Locate every leukocyte (white blood cell).
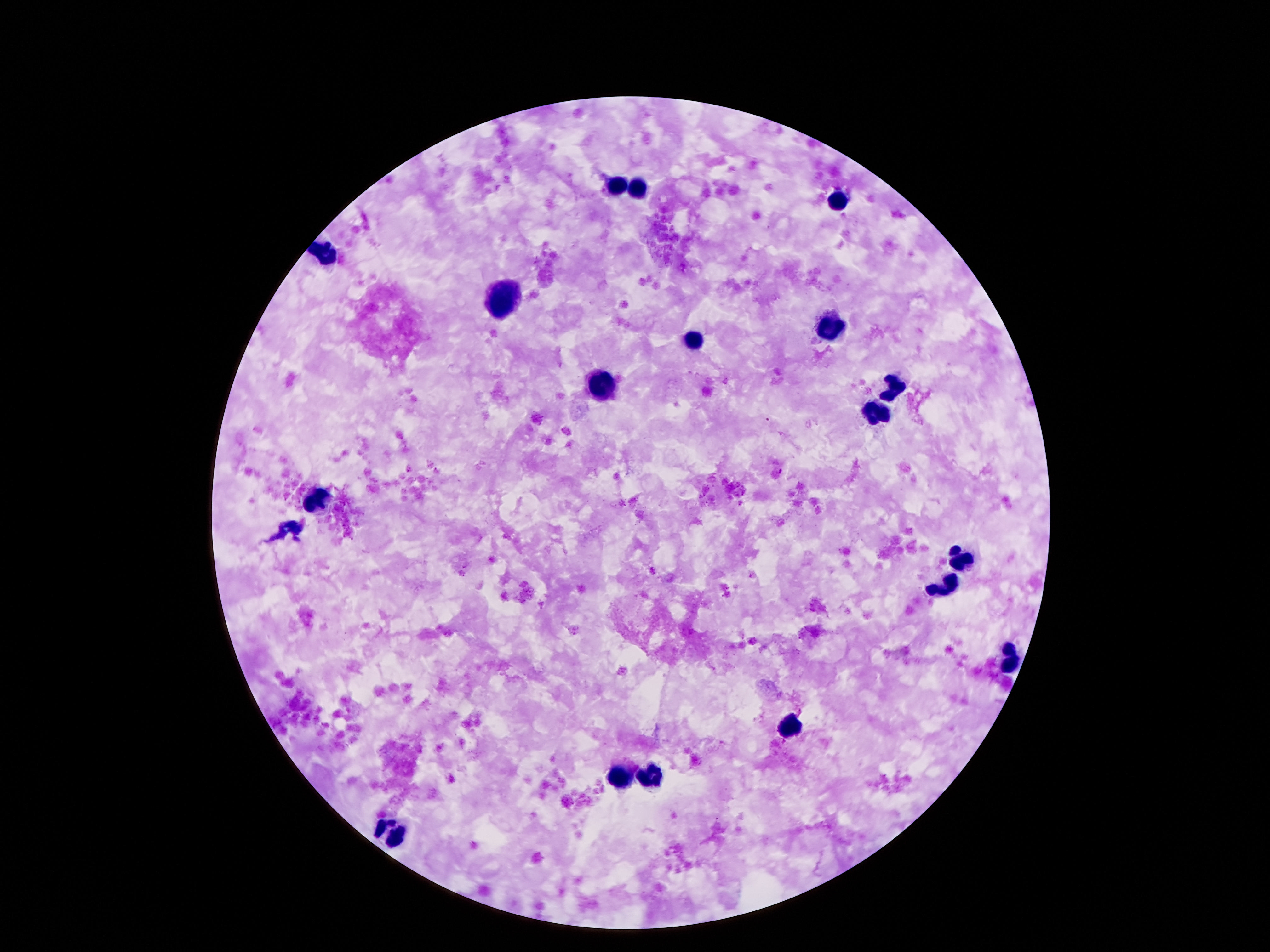
Approximate centers as {x, y} in pixels.
Leukocytes: {617, 184}, {635, 191}, {838, 201}, {326, 254}, {502, 303}, {828, 328}, {695, 337}, {601, 387}, {893, 387}, {875, 412}, {318, 500}, {961, 561}, {943, 582}, {1010, 659}, {789, 732}, {652, 775}, {619, 777}, {390, 832}.

100x magnification. Image is 1270×952 pixels. Patient malaria status: not infected. Thick peripheral-blood smear. Photographed through the microscope eyepiece with a smartphone camera. One field from this slide. Giemsa stain.